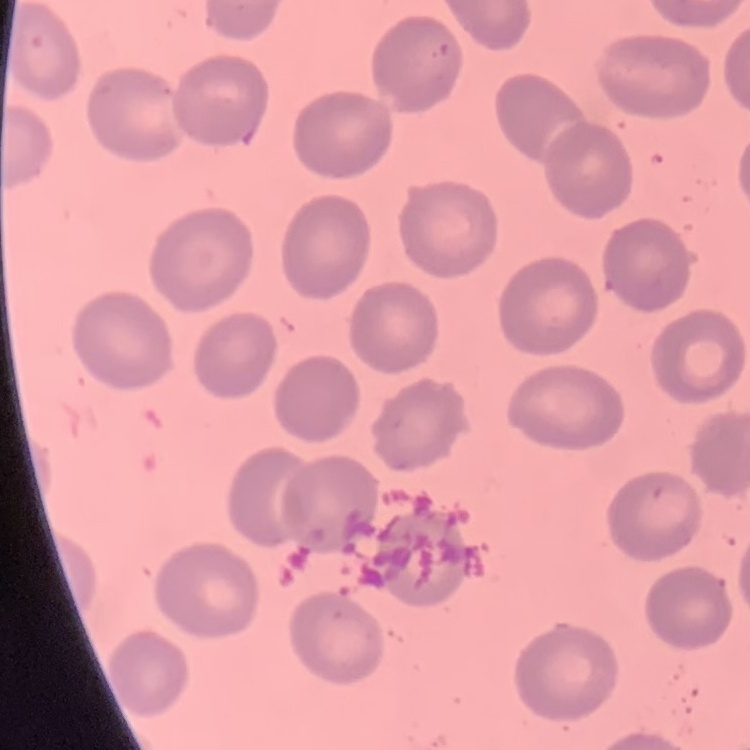
The red blood cells show no rouleaux formation. Square crop of a larger photomicrograph. Thin blood smear. Stained with either Field's or Giemsa.